Report the malaria status of this cell.
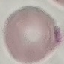

Uninfected.

capture = smartphone through the microscope eyepiece
preparation = thin blood film
image type = automatically extracted cell patch, resized to 64 × 64 pixels
stain = Giemsa